Point out each Plasmodium parasite.
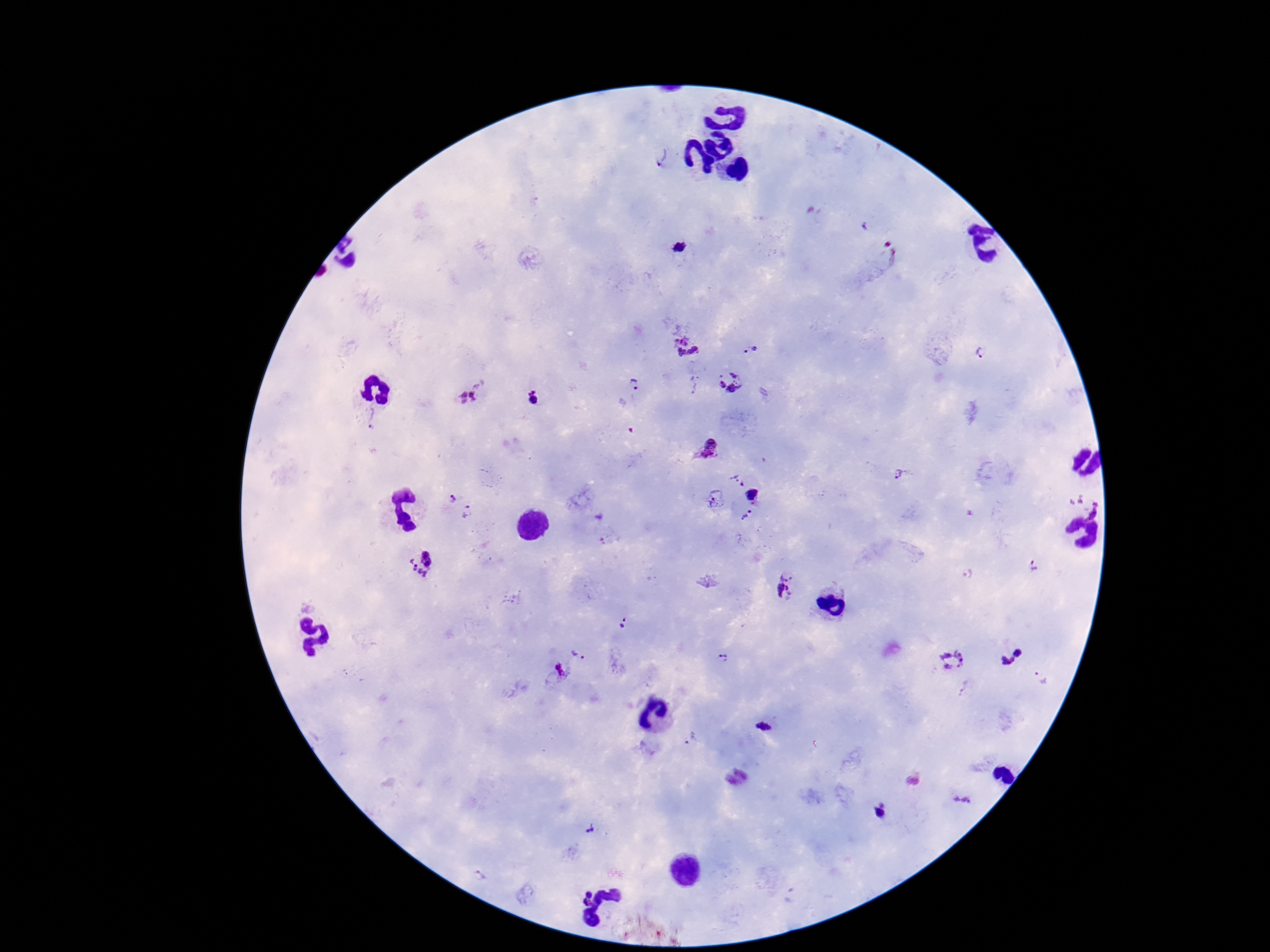

Approximate centers as [x, y] in pixels.
Plasmodium parasites: [659, 156], [680, 248], [878, 255], [686, 344], [751, 351], [983, 351], [731, 382], [635, 384], [467, 398], [535, 398], [371, 419], [708, 449], [901, 474], [738, 479], [753, 494], [450, 498], [715, 499], [1087, 506], [470, 512], [747, 517], [420, 563], [1035, 563], [965, 575], [785, 586], [621, 624], [579, 654], [720, 659], [1011, 660], [954, 662], [556, 674], [1042, 676], [764, 727], [690, 740], [913, 781], [961, 798], [880, 812], [588, 829].

Summary:
  - Stain: Giemsa
  - Field of view: single
  - Image size: 1270×952 pixels
  - Preparation: thick blood smear
  - Magnification: 100x
  - Capture: smartphone camera through the microscope eyepiece
  - Patient malaria status: infected